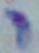

identification: Toxoplasma gondii
magnification: 1000x
modality: photomicrograph